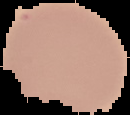
From a thin blood smear. The area outside the segmented cell region is set to black. Image is 130×115 pixels. Malaria status: uninfected.